Assess this cell for malaria.
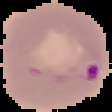
Parasitized.

Image is 112×112 pixels. Segmented cell region on a black background. From a thin blood smear.